Report the malaria status of this cell.
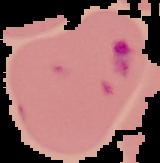

It is parasitized.

Image is 160×163 pixels. Cell region segmented out of the field of view; the surrounding area is masked to black. From a thin blood film.